Identify the preparation type.
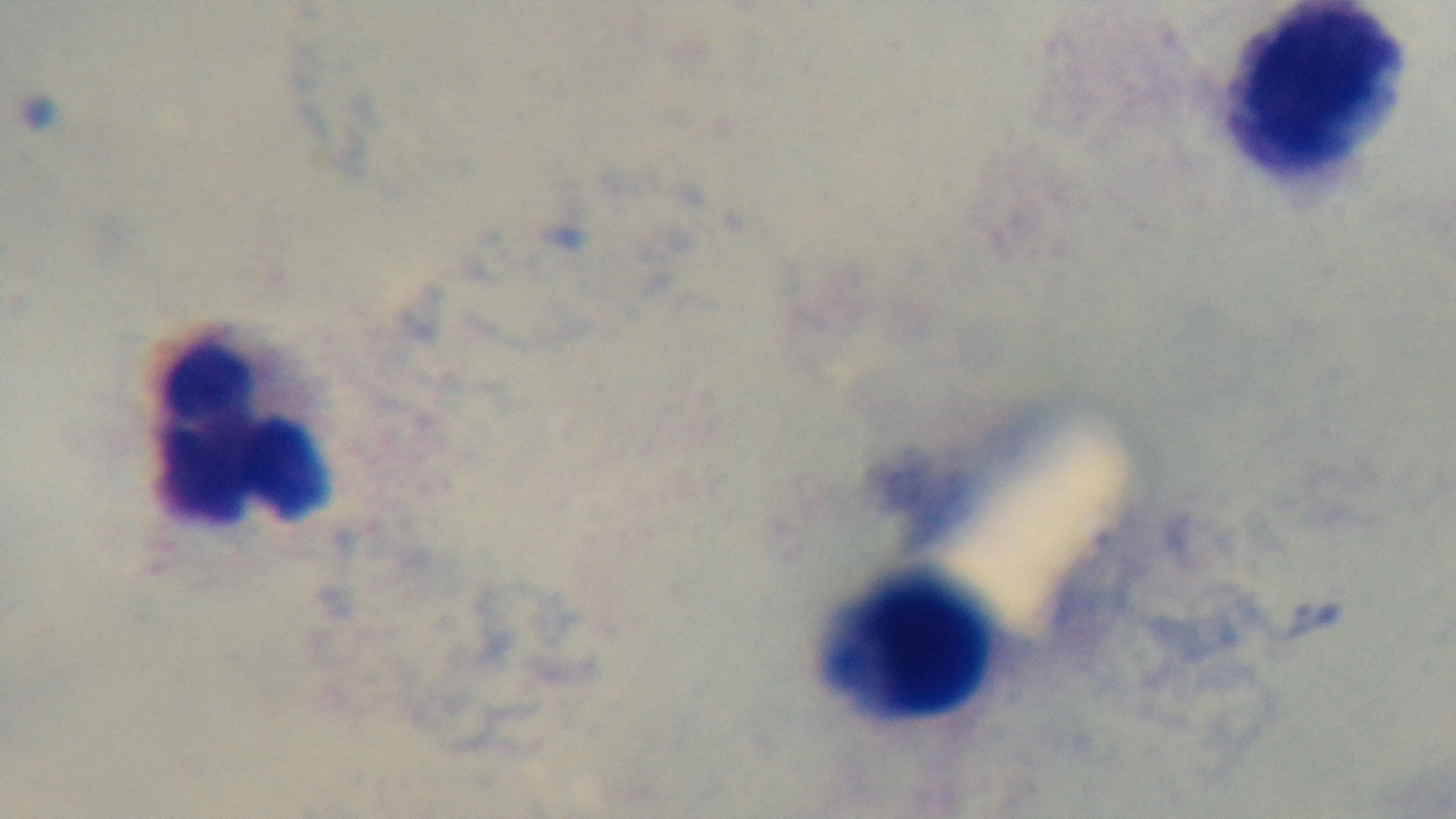
Thick.

{
  "modality": "light microscopy",
  "stain": "Giemsa",
  "objective": "100x oil immersion",
  "capture": "mounted 4K digital camera",
  "field_of_view": "single",
  "malaria_status": "uninfected"
}